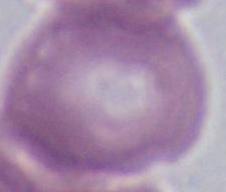

Summary:
  - Identification: red blood cell
  - Modality: micrograph
  - Magnification: 1000x